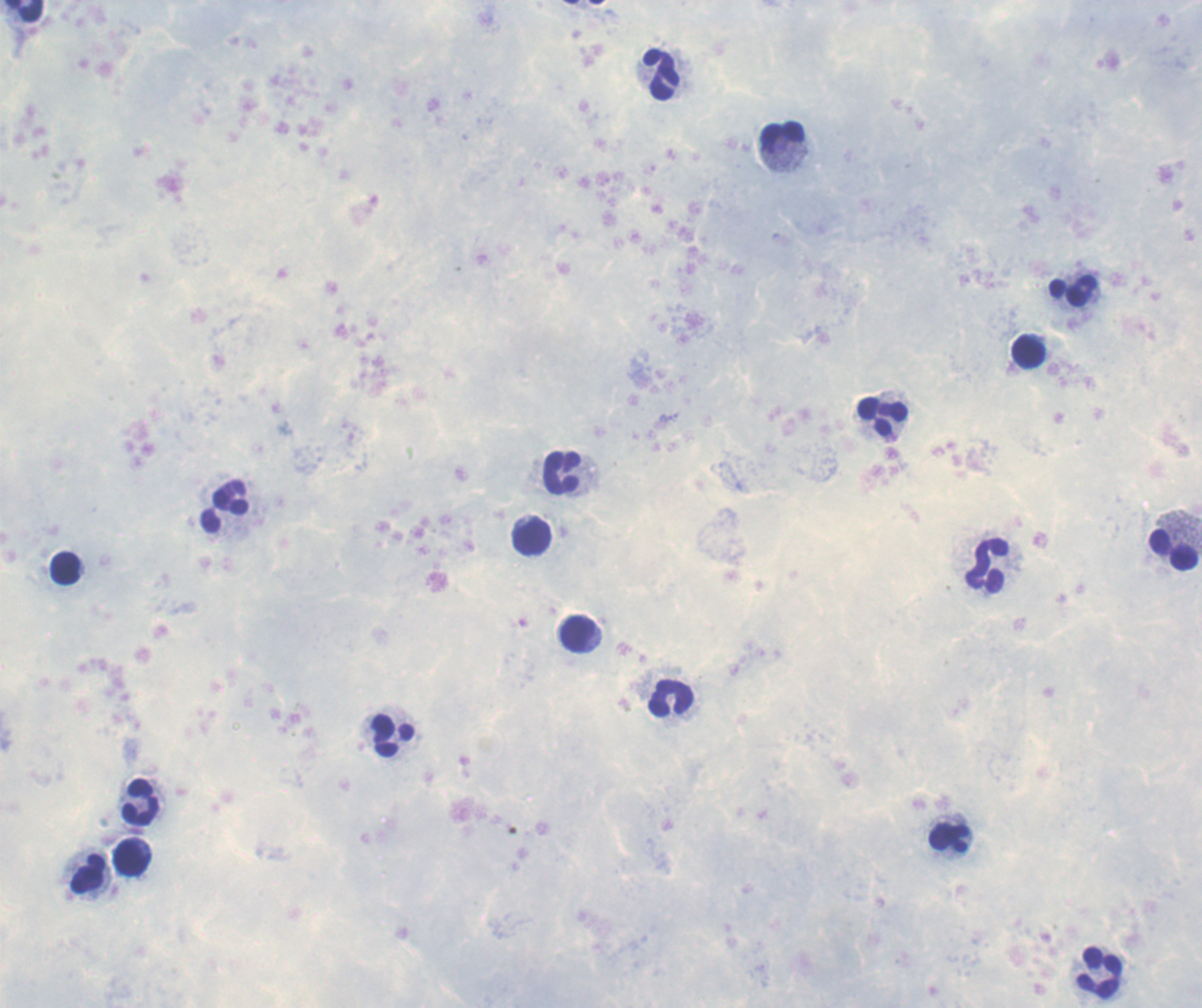

Approximate object centers, in pixels from the top-left corner. Leukocyte locations: (x=22, y=11), (x=660, y=74), (x=782, y=133), (x=1073, y=291), (x=1028, y=350), (x=883, y=415), (x=562, y=473), (x=224, y=505), (x=531, y=537), (x=1173, y=549), (x=988, y=565), (x=65, y=568), (x=577, y=633), (x=670, y=698), (x=393, y=736), (x=140, y=803), (x=948, y=837), (x=132, y=857), (x=89, y=874), (x=1099, y=972). Result: no malaria parasites seen. Romanowsky-stained preparation. Single field of view. Previously used in a real diagnosis. Thick blood film. Captured at 100x magnification. Image is 1202×1008 pixels. Background quality: poor.